Locate and identify every blood parasite.
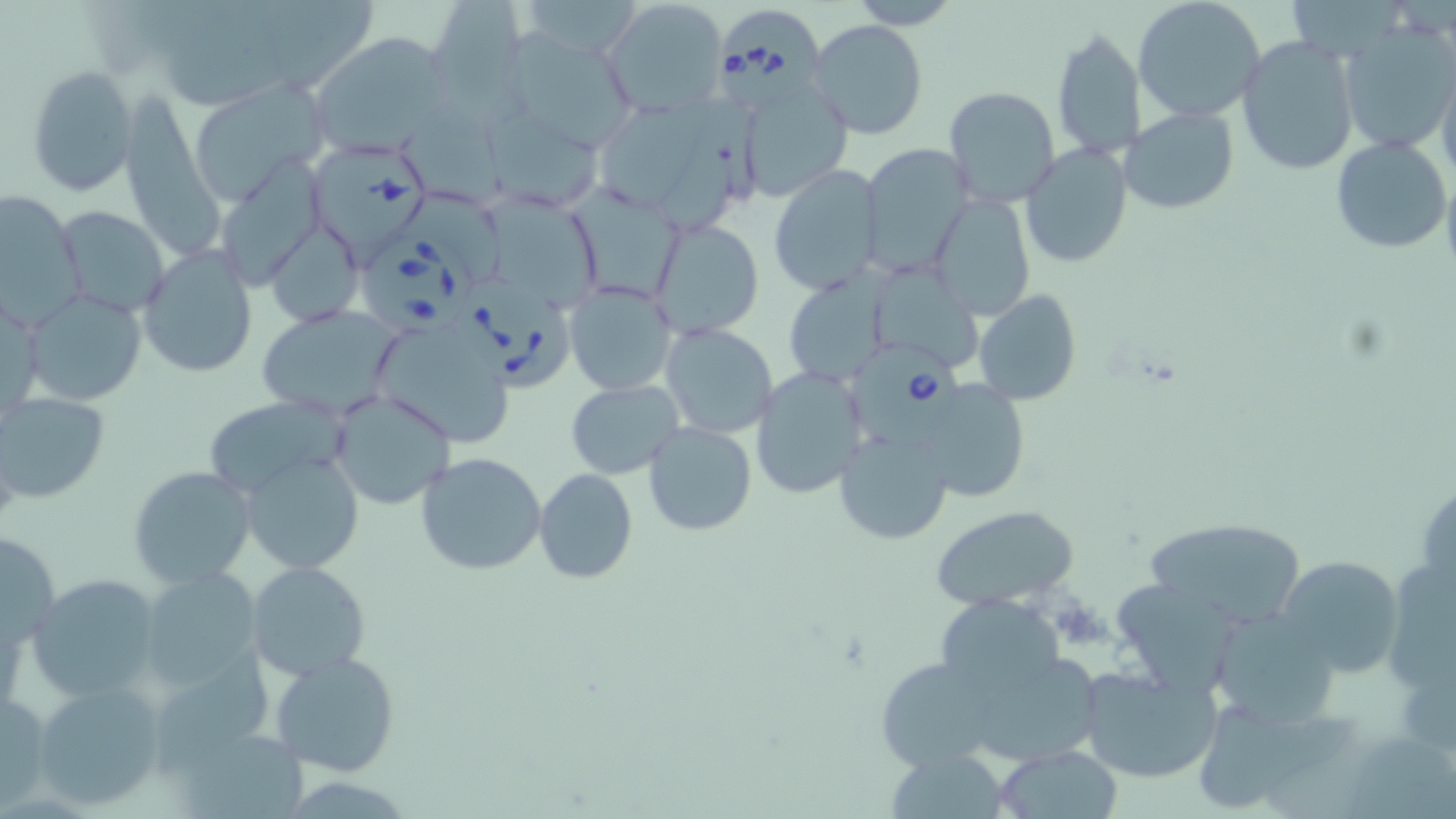

Approximate bounding boxes as named x1/y1/x2/y2 corners in pixels.
Babesia divergens-infected red blood cells: (x1=718, y1=4, x2=826, y2=109), (x1=310, y1=141, x2=433, y2=268), (x1=359, y1=235, x2=478, y2=335), (x1=456, y1=275, x2=572, y2=397), (x1=849, y1=344, x2=963, y2=448).
No Plasmodium falciparum, Plasmodium ovale, Plasmodium malariae, Plasmodium vivax, or Trypanosoma brucei observed.

Uninfected red blood cell locations: (x1=428, y1=0, x2=526, y2=102), (x1=600, y1=0, x2=729, y2=117), (x1=847, y1=0, x2=964, y2=29), (x1=1133, y1=0, x2=1266, y2=122), (x1=809, y1=19, x2=929, y2=139), (x1=1341, y1=22, x2=1456, y2=153), (x1=1050, y1=28, x2=1143, y2=162), (x1=316, y1=32, x2=453, y2=153), (x1=507, y1=32, x2=639, y2=153), (x1=1237, y1=36, x2=1359, y2=176), (x1=1437, y1=63, x2=1456, y2=190), (x1=27, y1=64, x2=139, y2=196), (x1=734, y1=72, x2=852, y2=202), (x1=186, y1=82, x2=331, y2=204), (x1=942, y1=87, x2=1062, y2=210), (x1=127, y1=93, x2=224, y2=253), (x1=479, y1=99, x2=602, y2=212), (x1=1121, y1=106, x2=1238, y2=213), (x1=1331, y1=134, x2=1452, y2=255), (x1=862, y1=142, x2=976, y2=276), (x1=1020, y1=143, x2=1133, y2=269), (x1=218, y1=159, x2=328, y2=295), (x1=768, y1=164, x2=881, y2=297), (x1=568, y1=186, x2=686, y2=306), (x1=0, y1=189, x2=86, y2=334), (x1=929, y1=194, x2=1037, y2=320), (x1=482, y1=197, x2=610, y2=311), (x1=54, y1=205, x2=172, y2=316), (x1=648, y1=217, x2=765, y2=340), (x1=270, y1=220, x2=365, y2=321), (x1=137, y1=243, x2=257, y2=378), (x1=881, y1=268, x2=981, y2=372), (x1=786, y1=272, x2=886, y2=387), (x1=564, y1=281, x2=678, y2=397), (x1=0, y1=289, x2=42, y2=427), (x1=974, y1=289, x2=1082, y2=406), (x1=22, y1=290, x2=146, y2=406), (x1=256, y1=304, x2=407, y2=420), (x1=660, y1=323, x2=777, y2=437), (x1=370, y1=331, x2=511, y2=443), (x1=751, y1=366, x2=869, y2=500), (x1=914, y1=376, x2=1033, y2=503), (x1=567, y1=379, x2=685, y2=478), (x1=329, y1=390, x2=456, y2=510), (x1=0, y1=393, x2=110, y2=503), (x1=202, y1=396, x2=351, y2=502), (x1=644, y1=422, x2=757, y2=535), (x1=833, y1=428, x2=954, y2=546), (x1=415, y1=451, x2=548, y2=575), (x1=245, y1=453, x2=365, y2=574), (x1=128, y1=466, x2=256, y2=590), (x1=534, y1=468, x2=638, y2=583), (x1=930, y1=504, x2=1081, y2=611), (x1=1142, y1=517, x2=1306, y2=629), (x1=1, y1=529, x2=58, y2=656), (x1=1276, y1=555, x2=1404, y2=679), (x1=248, y1=561, x2=369, y2=680), (x1=136, y1=566, x2=266, y2=692), (x1=1388, y1=566, x2=1454, y2=697), (x1=28, y1=575, x2=163, y2=705), (x1=1120, y1=582, x2=1230, y2=695), (x1=928, y1=594, x2=1070, y2=711), (x1=1208, y1=611, x2=1339, y2=727), (x1=269, y1=649, x2=401, y2=776), (x1=868, y1=653, x2=1021, y2=773), (x1=994, y1=656, x2=1103, y2=762), (x1=160, y1=661, x2=277, y2=769), (x1=1078, y1=664, x2=1223, y2=784), (x1=31, y1=681, x2=167, y2=810), (x1=0, y1=686, x2=52, y2=808), (x1=1201, y1=713, x2=1367, y2=812), (x1=187, y1=724, x2=319, y2=816), (x1=1359, y1=735, x2=1456, y2=819), (x1=995, y1=745, x2=1124, y2=818), (x1=889, y1=754, x2=1010, y2=819). Slide-level diagnosis: Babesia divergens. Image is 1456×819 pixels. One field of a larger specimen. Captured at 1000x magnification. Optical microscopy. Thin blood smear. May-Grünwald-Giemsa-stained preparation.